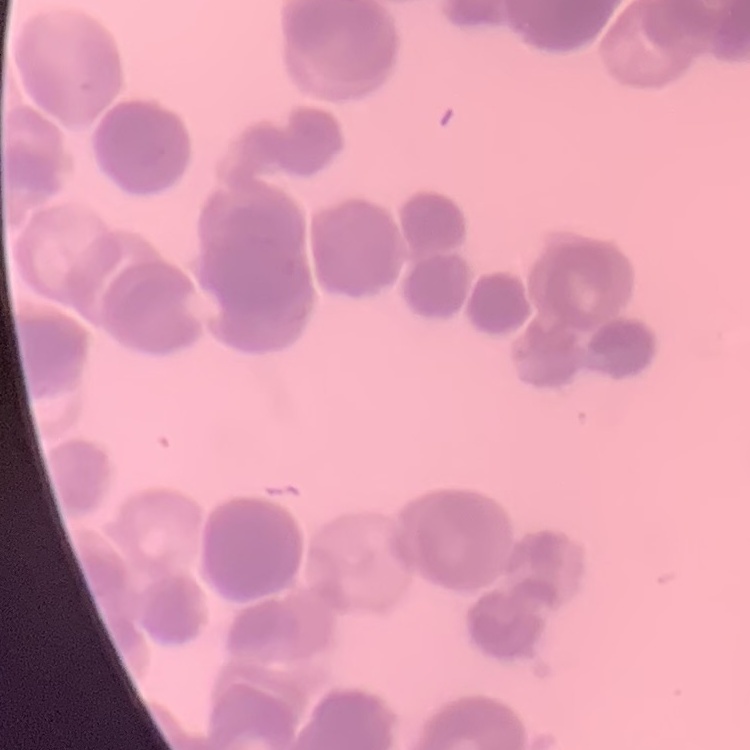

The erythrocytes exhibit rouleaux formation. Thin peripheral smear. Stained with either Field's or Giemsa. One tile cut from a larger photomicrograph.